Classify this cell by malaria status.
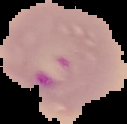
It is parasitized.

Summary:
  - Image type: segmented cell region with the area outside set to black
  - Preparation: thin blood smear
  - Image size: 127×124 pixels